Locate every blood parasite and identify its species.
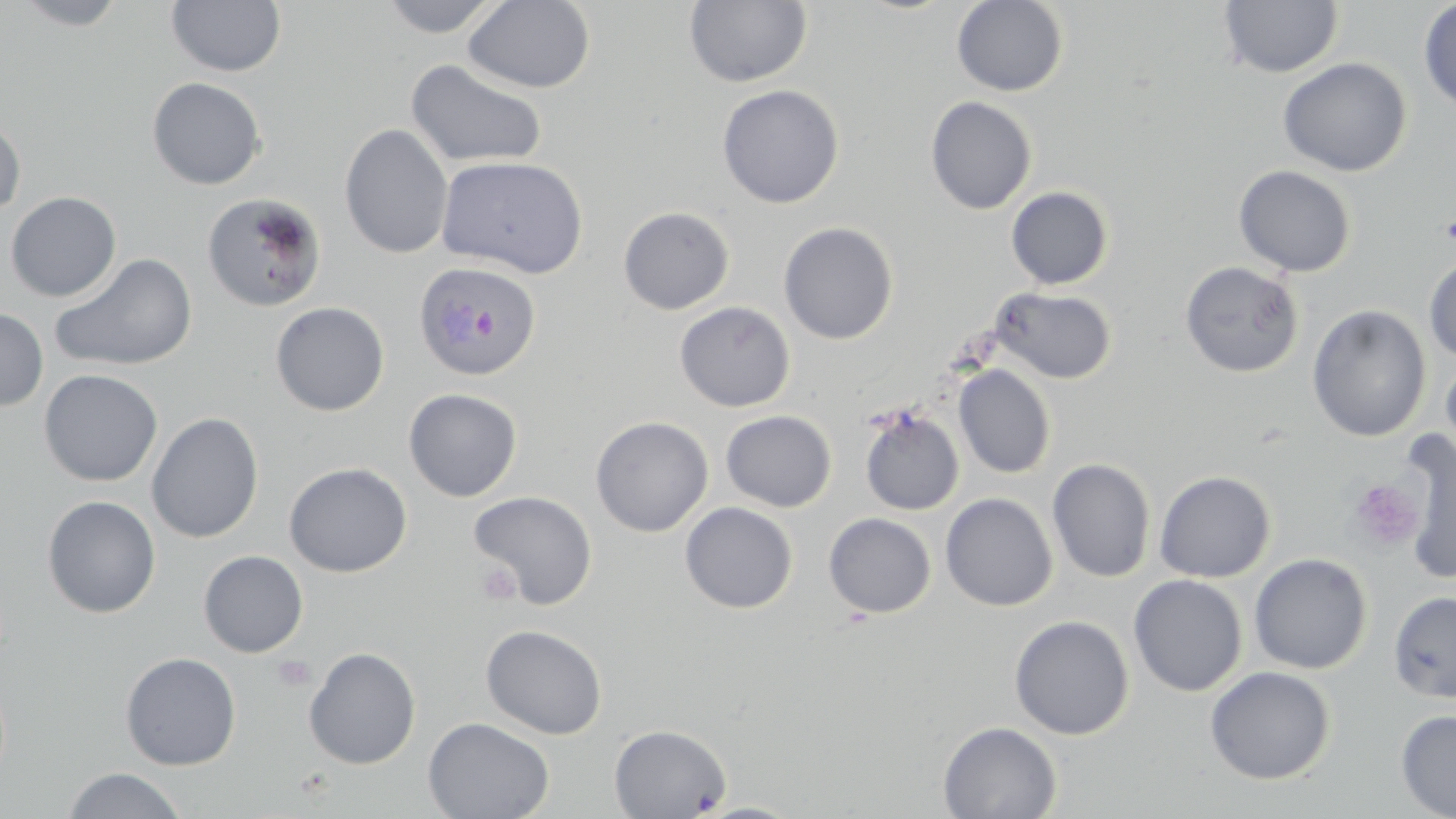
Approximate bounding boxes as named x1/y1/x2/y2 corners in pixels.
Plasmodium ovale-infected red blood cells: (x1=413, y1=260, x2=542, y2=381).
No Plasmodium falciparum, Plasmodium malariae, Plasmodium vivax, Babesia divergens, or Trypanosoma brucei observed.

Platelet locations: (x1=1348, y1=479, x2=1424, y2=551), (x1=476, y1=561, x2=521, y2=606), (x1=272, y1=655, x2=315, y2=692). Uninfected red blood cell locations: (x1=11, y1=0, x2=131, y2=30), (x1=377, y1=0, x2=506, y2=37), (x1=463, y1=0, x2=596, y2=93), (x1=683, y1=0, x2=813, y2=89), (x1=951, y1=0, x2=1069, y2=96), (x1=1418, y1=0, x2=1456, y2=115), (x1=166, y1=1, x2=287, y2=77), (x1=1218, y1=1, x2=1344, y2=78), (x1=1277, y1=57, x2=1412, y2=176), (x1=406, y1=58, x2=548, y2=169), (x1=147, y1=77, x2=266, y2=190), (x1=717, y1=84, x2=844, y2=208), (x1=925, y1=95, x2=1037, y2=215), (x1=0, y1=116, x2=25, y2=218), (x1=339, y1=123, x2=453, y2=259), (x1=436, y1=155, x2=588, y2=279), (x1=1234, y1=165, x2=1357, y2=277), (x1=1006, y1=186, x2=1114, y2=290), (x1=5, y1=191, x2=121, y2=301), (x1=202, y1=192, x2=327, y2=313), (x1=618, y1=206, x2=735, y2=314), (x1=779, y1=221, x2=899, y2=344), (x1=50, y1=253, x2=198, y2=372), (x1=1423, y1=253, x2=1456, y2=364), (x1=1179, y1=260, x2=1304, y2=378), (x1=990, y1=286, x2=1117, y2=384), (x1=270, y1=301, x2=390, y2=416), (x1=674, y1=301, x2=796, y2=412), (x1=1307, y1=304, x2=1431, y2=442), (x1=0, y1=307, x2=48, y2=412), (x1=1440, y1=351, x2=1456, y2=468), (x1=953, y1=364, x2=1056, y2=479), (x1=38, y1=369, x2=163, y2=486), (x1=403, y1=388, x2=522, y2=502), (x1=858, y1=404, x2=965, y2=516), (x1=720, y1=410, x2=837, y2=512), (x1=146, y1=412, x2=264, y2=544), (x1=591, y1=416, x2=714, y2=536), (x1=1397, y1=429, x2=1455, y2=585), (x1=1046, y1=458, x2=1156, y2=582), (x1=284, y1=462, x2=411, y2=577), (x1=1154, y1=470, x2=1276, y2=583), (x1=470, y1=491, x2=598, y2=609), (x1=940, y1=492, x2=1058, y2=611), (x1=42, y1=495, x2=161, y2=618), (x1=680, y1=502, x2=798, y2=613), (x1=823, y1=512, x2=936, y2=618), (x1=198, y1=550, x2=308, y2=657), (x1=1248, y1=553, x2=1372, y2=674), (x1=1129, y1=574, x2=1248, y2=697), (x1=1388, y1=590, x2=1456, y2=702), (x1=1009, y1=615, x2=1134, y2=740), (x1=481, y1=624, x2=607, y2=740), (x1=303, y1=647, x2=421, y2=769), (x1=120, y1=651, x2=241, y2=770), (x1=1205, y1=666, x2=1336, y2=784), (x1=1395, y1=709, x2=1456, y2=818), (x1=423, y1=717, x2=554, y2=819), (x1=938, y1=721, x2=1062, y2=819), (x1=609, y1=724, x2=731, y2=818), (x1=61, y1=767, x2=189, y2=818), (x1=693, y1=802, x2=805, y2=818). Slide-level diagnosis: Plasmodium ovale. Thin blood film. Image is 1456×819 pixels. One field of a larger specimen. Optical microscopy. Captured at 1000x magnification. May-Grünwald-Giemsa-stained preparation.